Assess this cell for malaria.
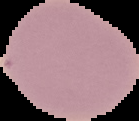
It is uninfected.

image_type: segmented cell region on a black background
image_size: 139×121 pixels
preparation: thin blood smear